Locate every blood parasite and identify its species.
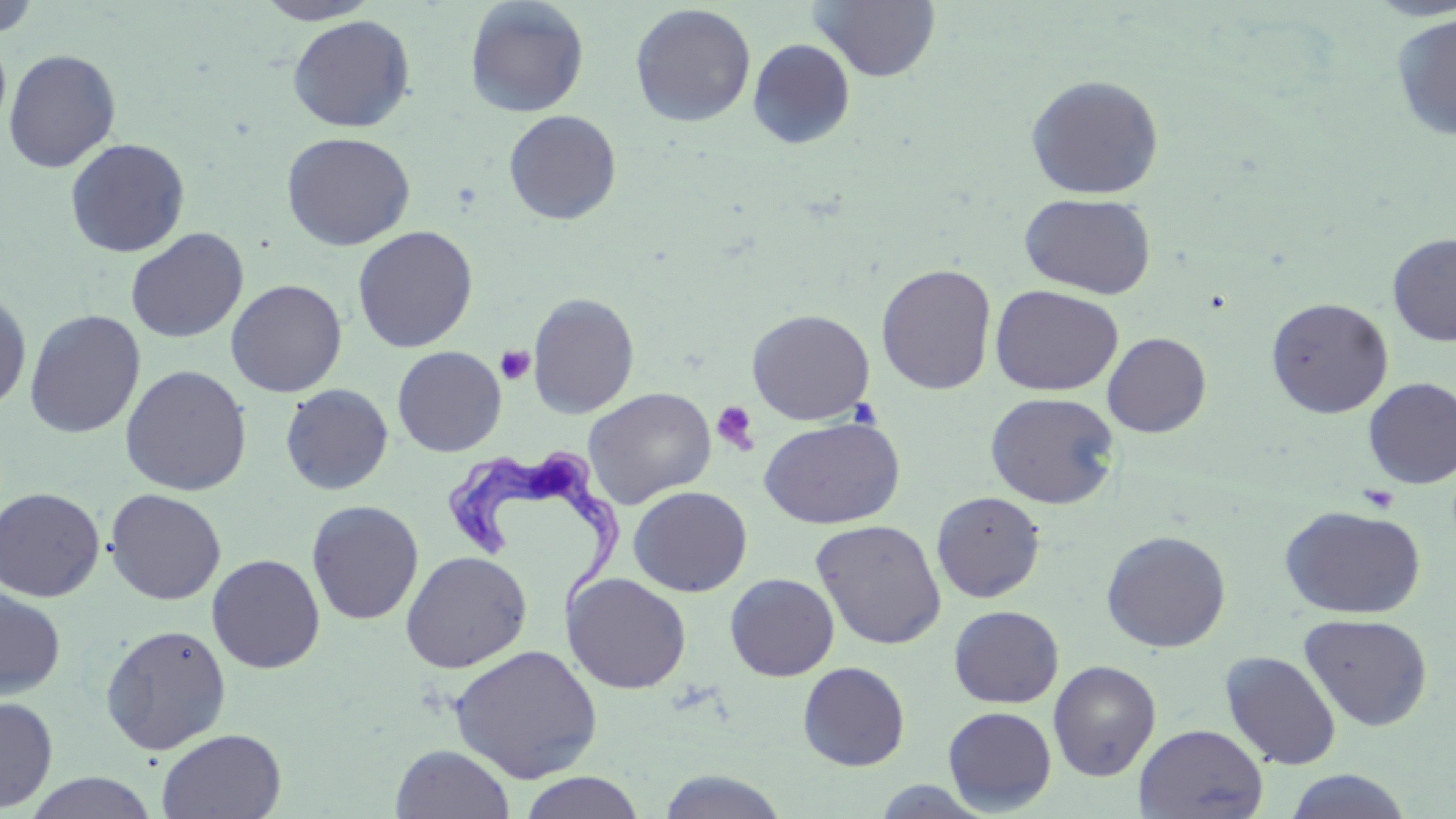

Approximate bounding boxes as named x1/y1/x2/y2 corners in pixels.
Trypanosoma brucei: (x1=441, y1=450, x2=627, y2=616).
No Plasmodium falciparum, Plasmodium ovale, Plasmodium malariae, Plasmodium vivax, or Babesia divergens observed.

slide-level diagnosis = Trypanosoma brucei
modality = light microscopy
platelet locations = approximate bounding boxes as named x1/y1/x2/y2 corners in pixels: (x1=496, y1=345, x2=535, y2=385), (x1=711, y1=400, x2=760, y2=455), (x1=1357, y1=484, x2=1399, y2=514)
preparation = thin blood film
image size = 1456×819 pixels
uninfected red blood cell locations = approximate bounding boxes as named x1/y1/x2/y2 corners in pixels: (x1=253, y1=0, x2=382, y2=25), (x1=809, y1=0, x2=942, y2=82), (x1=0, y1=1, x2=42, y2=39), (x1=464, y1=1, x2=589, y2=118), (x1=629, y1=4, x2=756, y2=127), (x1=1391, y1=12, x2=1456, y2=143), (x1=287, y1=15, x2=415, y2=132), (x1=0, y1=32, x2=12, y2=135), (x1=747, y1=38, x2=856, y2=149), (x1=3, y1=49, x2=121, y2=174), (x1=1024, y1=74, x2=1164, y2=200), (x1=503, y1=109, x2=622, y2=225), (x1=281, y1=131, x2=415, y2=251), (x1=64, y1=137, x2=191, y2=258), (x1=1019, y1=192, x2=1157, y2=299), (x1=353, y1=226, x2=478, y2=352), (x1=125, y1=227, x2=249, y2=344), (x1=1387, y1=233, x2=1456, y2=346), (x1=876, y1=263, x2=997, y2=395), (x1=225, y1=278, x2=348, y2=398), (x1=990, y1=284, x2=1124, y2=396), (x1=0, y1=289, x2=32, y2=412), (x1=528, y1=292, x2=639, y2=419), (x1=1266, y1=296, x2=1394, y2=418), (x1=747, y1=308, x2=875, y2=425), (x1=24, y1=309, x2=146, y2=439), (x1=1102, y1=332, x2=1212, y2=437), (x1=392, y1=346, x2=507, y2=457), (x1=119, y1=364, x2=252, y2=496), (x1=1363, y1=377, x2=1456, y2=488), (x1=280, y1=383, x2=394, y2=496), (x1=583, y1=387, x2=717, y2=509), (x1=985, y1=392, x2=1120, y2=509), (x1=759, y1=417, x2=905, y2=529), (x1=628, y1=485, x2=752, y2=597), (x1=0, y1=487, x2=105, y2=602), (x1=104, y1=488, x2=227, y2=605), (x1=931, y1=490, x2=1046, y2=602), (x1=306, y1=500, x2=424, y2=625), (x1=1279, y1=505, x2=1426, y2=619), (x1=810, y1=518, x2=947, y2=649), (x1=1101, y1=530, x2=1231, y2=652), (x1=400, y1=550, x2=532, y2=673), (x1=207, y1=553, x2=325, y2=674), (x1=562, y1=572, x2=691, y2=694), (x1=725, y1=573, x2=839, y2=681), (x1=0, y1=587, x2=66, y2=700), (x1=948, y1=605, x2=1063, y2=708), (x1=1299, y1=613, x2=1434, y2=732), (x1=100, y1=623, x2=232, y2=755), (x1=448, y1=644, x2=603, y2=784), (x1=1221, y1=651, x2=1342, y2=770), (x1=1048, y1=660, x2=1161, y2=781), (x1=797, y1=661, x2=910, y2=771), (x1=0, y1=696, x2=58, y2=813), (x1=943, y1=706, x2=1057, y2=814), (x1=1134, y1=724, x2=1268, y2=818), (x1=156, y1=728, x2=286, y2=819), (x1=390, y1=744, x2=516, y2=818), (x1=1283, y1=769, x2=1413, y2=818), (x1=655, y1=770, x2=790, y2=819), (x1=22, y1=772, x2=159, y2=818), (x1=517, y1=772, x2=646, y2=818)
magnification = 1000x
stain = May-Grünwald-Giemsa
field of view = single